Locate and identify every blood parasite.
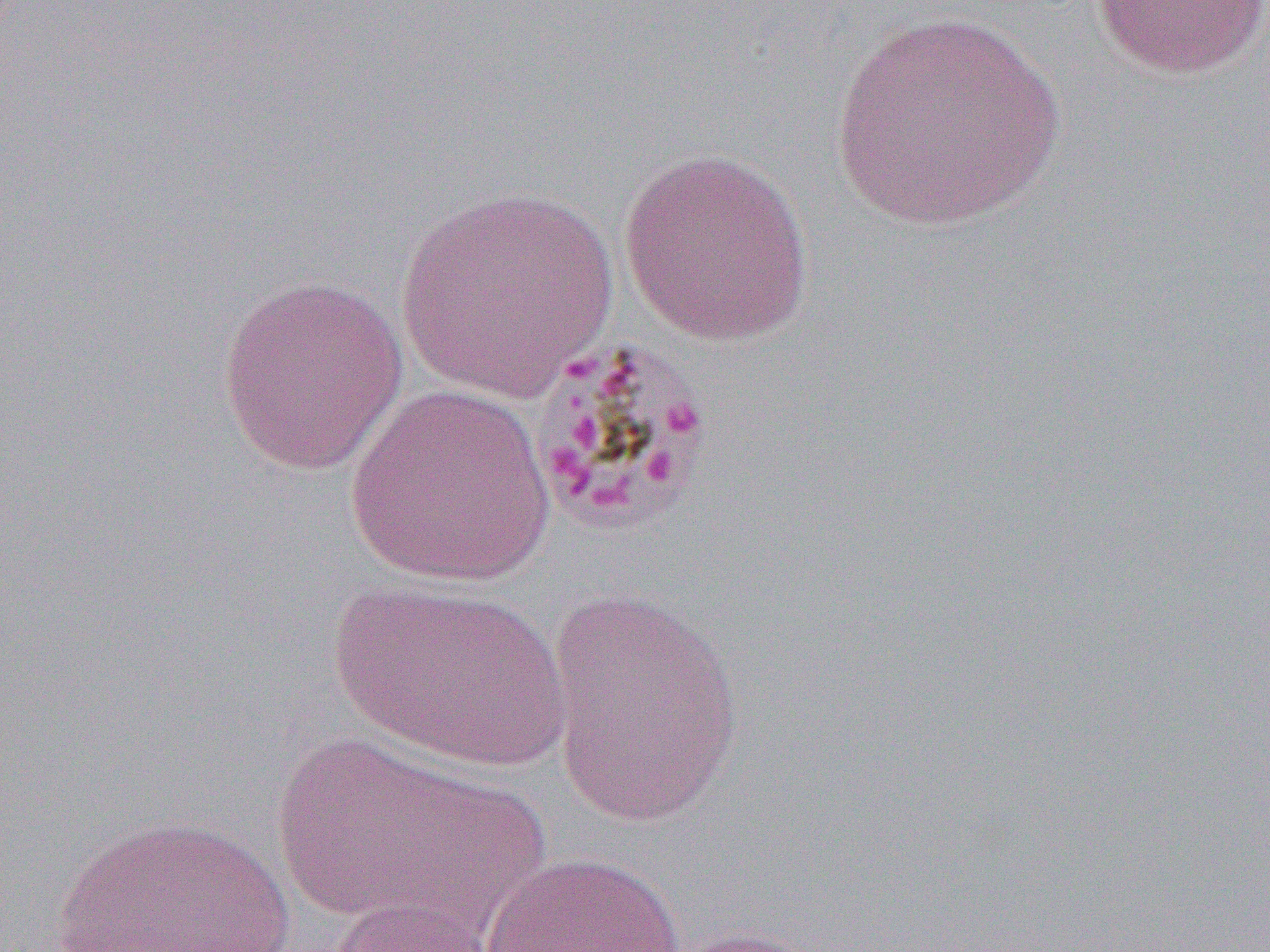

Approximate bounding boxes as (x1, y1, x2, y2) in pixels.
Plasmodium malariae-infected red blood cells: (523, 333, 717, 537).
No Plasmodium falciparum, Plasmodium ovale, Plasmodium vivax, Babesia divergens, or Trypanosoma brucei observed.

{
  "slide_level_diagnosis": "Plasmodium malariae",
  "image_size": "1270×952 pixels",
  "uninfected_red_blood_cell_locations": "approximate bounding boxes as (x1, y1, x2, y2) in pixels: (1090, 1, 1270, 80), (827, 11, 1068, 230), (619, 147, 816, 347), (393, 186, 619, 402), (215, 273, 409, 476), (342, 385, 557, 587), (328, 579, 571, 772), (544, 585, 745, 829), (262, 731, 540, 931), (54, 813, 292, 951), (475, 851, 693, 952), (326, 896, 505, 952), (653, 924, 837, 952)",
  "modality": "optical microscopy",
  "field_of_view": "single",
  "magnification": "1000x",
  "preparation": "thin blood film"
}